Assess this cell for malaria.
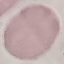

Uninfected.

capture: smartphone camera at the microscope eyepiece
stain: Giemsa
image_type: cell patch, automatically extracted from a larger field of view and resized to 64 × 64 pixels
preparation: thin smear